Give the extent of all Plasmodium falciparum-infected red blood cells.
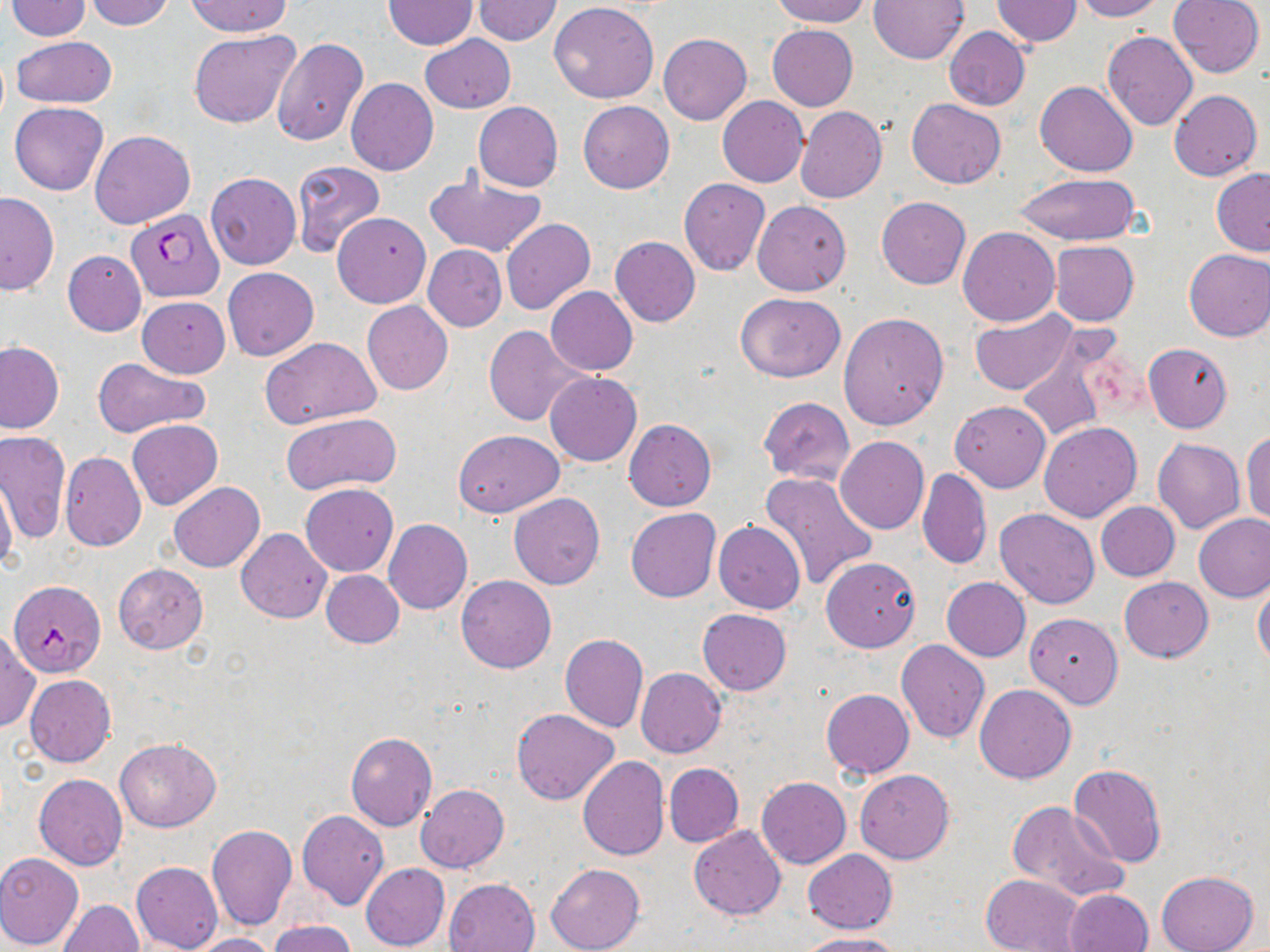

Approximate bounding boxes as (x1, y1, x2, y2) in pixels.
Plasmodium falciparum-infected red blood cells: (126, 209, 224, 302), (7, 579, 104, 677).

slide-level diagnosis = Plasmodium falciparum
stain = May-Grünwald-Giemsa
uninfected red blood cell locations = approximate bounding boxes as (x1, y1, x2, y2) in pixels: (84, 0, 178, 30), (185, 0, 294, 38), (471, 0, 563, 46), (771, 0, 870, 27), (867, 0, 968, 64), (991, 0, 1082, 47), (1070, 0, 1165, 21), (1167, 0, 1264, 78), (5, 1, 92, 40), (382, 1, 477, 50), (549, 1, 660, 103), (767, 24, 857, 111), (943, 27, 1030, 110), (189, 29, 300, 128), (1102, 31, 1197, 132), (658, 33, 751, 124), (420, 34, 516, 113), (11, 36, 117, 108), (271, 38, 368, 145), (345, 78, 438, 176), (1036, 81, 1137, 177), (1168, 88, 1261, 181), (718, 96, 808, 186), (906, 99, 1006, 189), (579, 101, 674, 193), (9, 102, 108, 195), (473, 102, 562, 192), (795, 106, 887, 204), (90, 130, 195, 229), (291, 160, 385, 258), (1211, 168, 1270, 256), (422, 170, 547, 258), (205, 172, 301, 270), (1014, 173, 1140, 247), (678, 178, 770, 276), (0, 192, 58, 296), (876, 197, 971, 289), (752, 200, 850, 296), (333, 211, 431, 308), (501, 218, 595, 314), (958, 225, 1060, 326), (610, 236, 700, 327), (1049, 241, 1140, 326), (424, 244, 506, 331), (1182, 248, 1270, 341), (63, 249, 147, 336), (222, 267, 318, 361), (544, 286, 637, 375), (734, 292, 846, 382), (137, 296, 230, 377), (362, 301, 453, 395), (968, 308, 1081, 398), (838, 313, 950, 430), (484, 324, 587, 426), (260, 336, 382, 429), (1016, 337, 1117, 443), (0, 340, 65, 434), (1143, 343, 1233, 432), (93, 359, 210, 438), (545, 372, 642, 466), (758, 398, 855, 484), (950, 400, 1051, 492), (281, 411, 403, 494), (127, 419, 224, 510), (624, 420, 716, 510), (1038, 421, 1142, 522), (453, 429, 563, 517), (1242, 429, 1270, 527), (1, 430, 70, 544), (835, 436, 928, 533), (1152, 437, 1245, 533), (60, 451, 146, 552), (917, 468, 991, 570), (759, 471, 880, 591), (0, 476, 18, 574), (169, 482, 265, 573), (300, 483, 398, 576), (509, 492, 604, 589), (1096, 502, 1180, 582), (626, 508, 720, 602), (994, 508, 1101, 609), (1193, 514, 1270, 603), (383, 519, 473, 614), (713, 521, 806, 613), (235, 528, 332, 622), (821, 556, 921, 652), (113, 563, 208, 653), (321, 570, 404, 647), (456, 574, 556, 673), (1119, 576, 1212, 662), (942, 577, 1031, 661), (1252, 579, 1270, 666), (698, 608, 792, 695), (1025, 613, 1123, 708), (0, 629, 39, 735), (559, 633, 649, 732), (895, 638, 990, 744), (635, 668, 726, 758), (24, 674, 116, 767), (979, 674, 1083, 878), (975, 684, 1077, 784), (821, 689, 914, 779), (512, 709, 619, 805), (345, 732, 437, 831), (116, 738, 220, 832), (577, 755, 669, 862), (664, 763, 744, 846), (673, 764, 757, 912), (1068, 764, 1167, 868), (855, 769, 955, 864), (34, 774, 128, 869), (756, 776, 851, 868), (416, 784, 509, 872), (1007, 800, 1130, 903), (297, 811, 391, 911), (205, 823, 296, 930), (688, 826, 786, 919), (804, 849, 897, 934), (0, 852, 84, 950), (132, 861, 222, 951), (361, 863, 449, 951), (547, 863, 644, 952), (1155, 871, 1259, 952), (981, 874, 1085, 952), (443, 878, 540, 952), (1063, 889, 1154, 952), (58, 899, 143, 951), (270, 920, 357, 952), (186, 932, 278, 952), (796, 934, 906, 952)
field of view = single
modality = light microscopy
magnification = 1000x
image size = 1270×952 pixels
preparation = thin blood smear